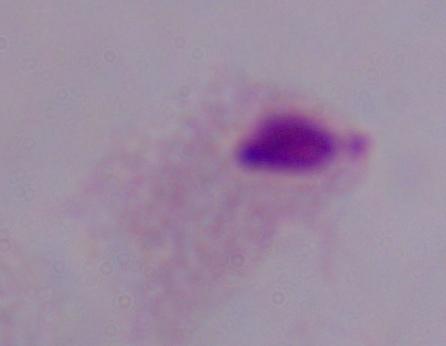

magnification: 1000x
modality: photomicrograph
identification: trichomonad